Classify this cell by malaria status.
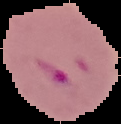
Parasitized.

From a thin blood film. Image is 121×124 pixels. Cell region segmented out of the field of view; the surrounding area is masked to black.